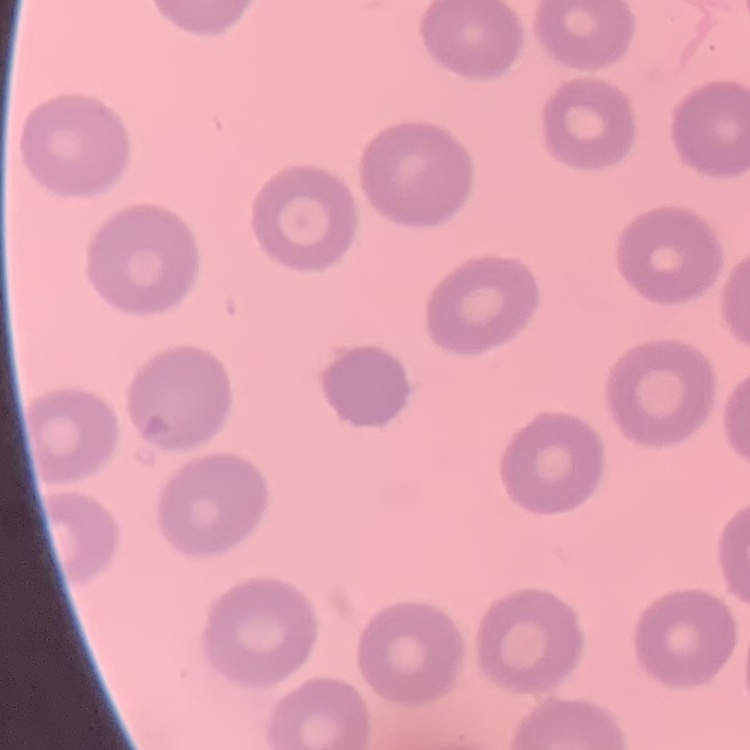

red blood cell morphology = no rouleaux formation
preparation = thin peripheral smear
image type = square crop of a larger photomicrograph
stain = Field's or Giemsa